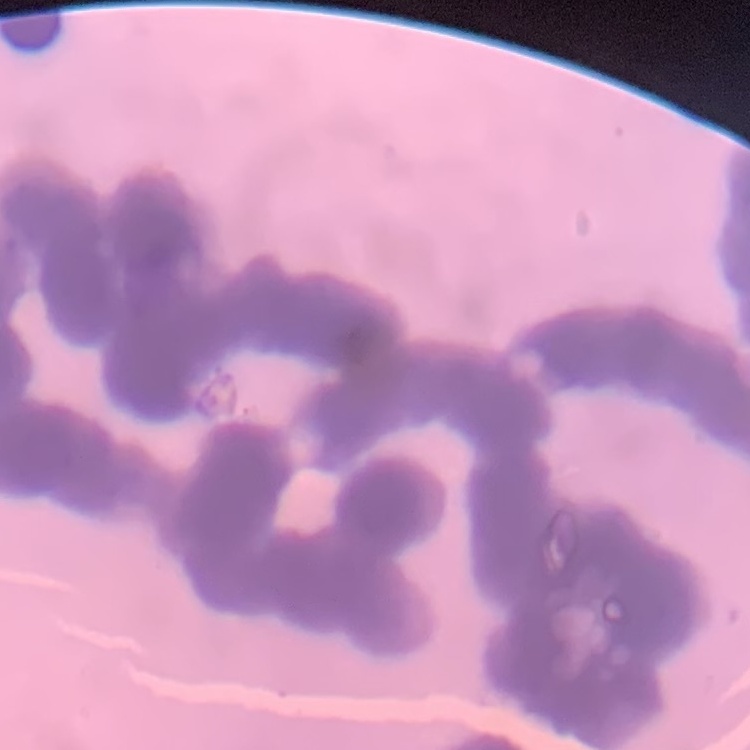

red blood cell morphology = rouleaux formation
image type = square crop of a larger photomicrograph
stain = Field's or Giemsa
preparation = thin blood film